Name the parasite shown.
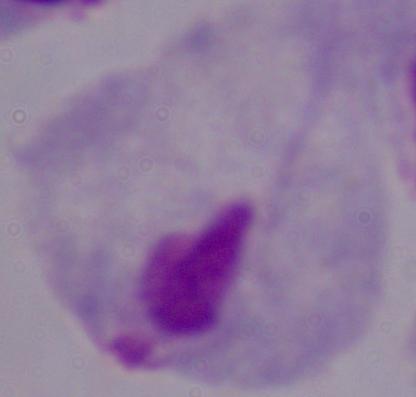
A trichomonad.

Photomicrograph. 1000x magnification.